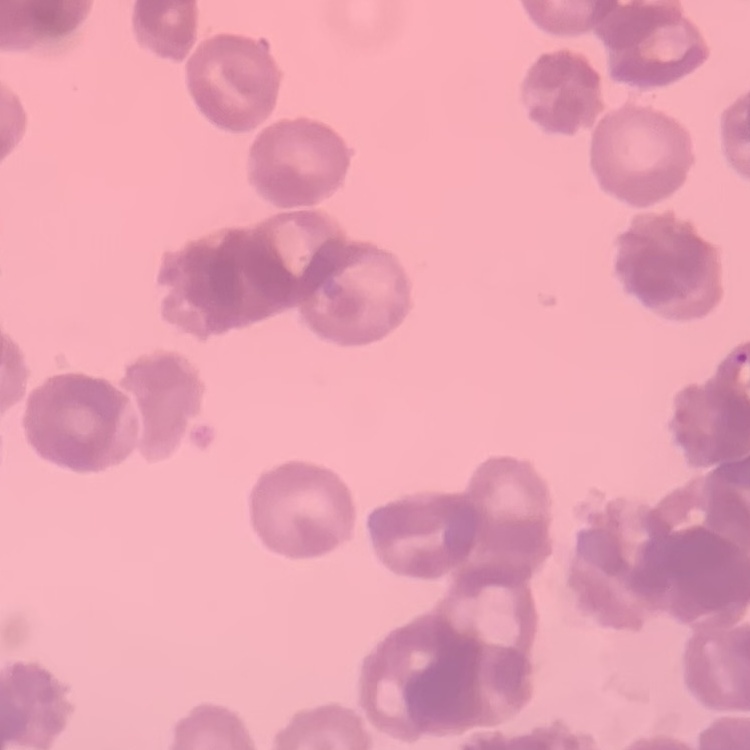

red blood cell morphology = rouleaux formation
stain = Field's or Giemsa
image type = square crop of a larger photomicrograph
preparation = thin blood smear